Identify the cell.
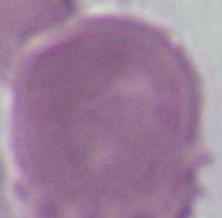
An erythrocyte.

Micrograph. Captured at 1000x magnification.